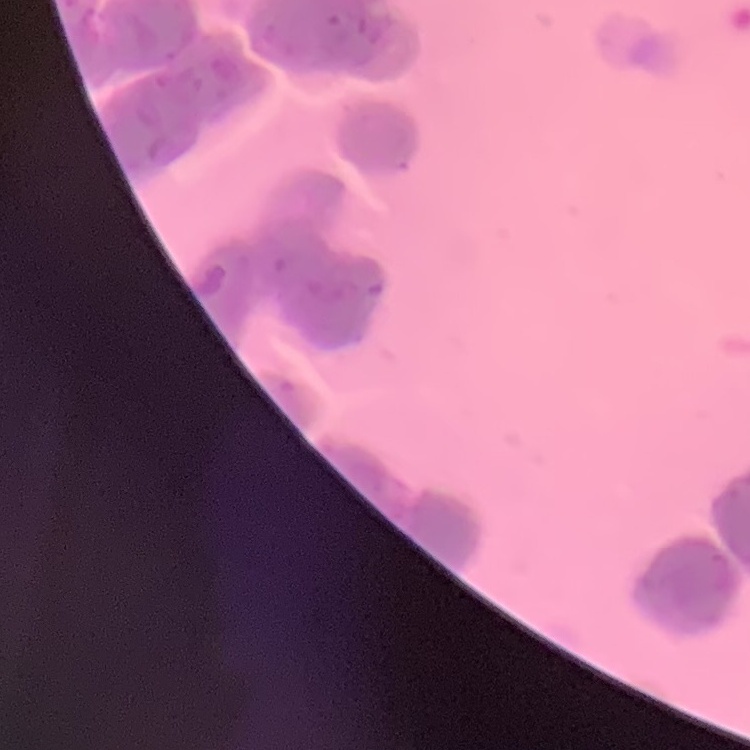

Summary:
  - Erythrocyte morphology: rouleaux formation
  - Image type: square crop of a larger photomicrograph
  - Preparation: thin peripheral smear
  - Stain: Field's or Giemsa